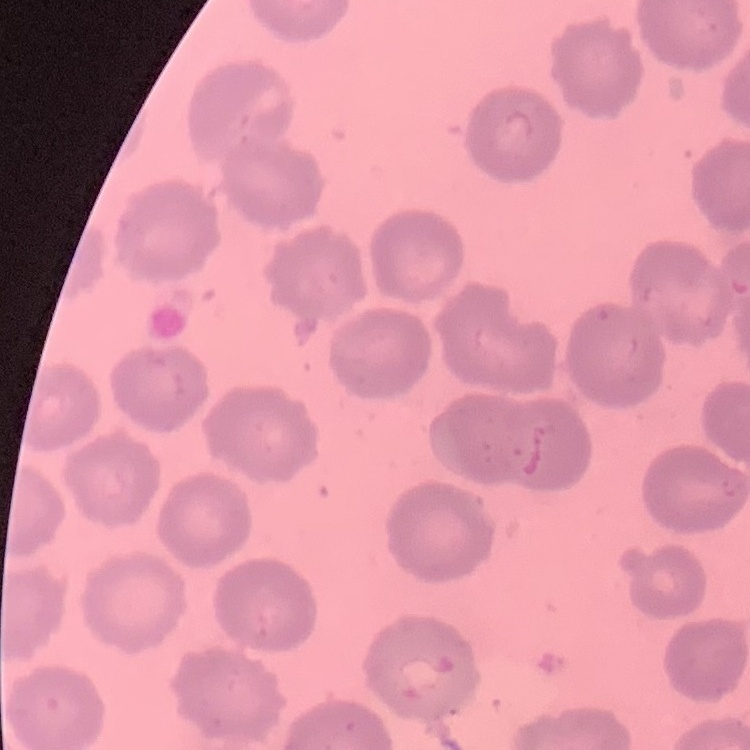

Summary:
  - Erythrocyte morphology: no rouleaux formation
  - Preparation: thin blood film
  - Stain: Field's or Giemsa
  - Image type: one tile cut from a larger photomicrograph